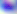

identification = Toxoplasma gondii
magnification = 400x
modality = micrograph